Report the malaria status of this cell.
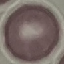

Uninfected.

stain: Giemsa
image_type: cell patch, automatically extracted from a larger field of view and resized to 64 × 64 pixels
preparation: thin blood smear
capture: smartphone through the microscope eyepiece